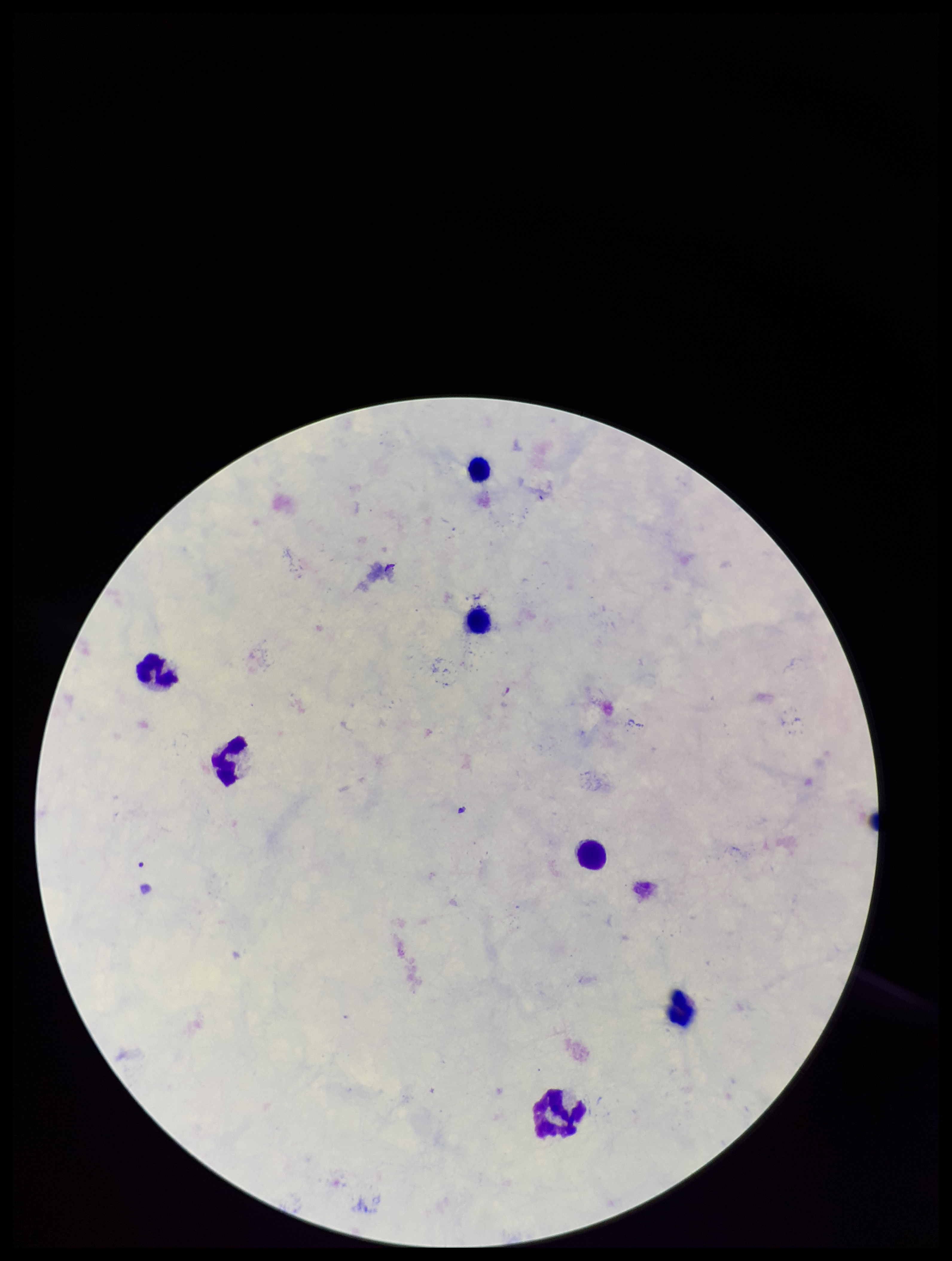

Image is 952×1261 pixels. Leukocyte count: 7. Stained with Giemsa. Patient malaria status: positive. Plasmodium parasites: none detected. Preparation: thick. Parasite count: 0. Single field of view. Species reported for this patient: Plasmodium falciparum. Smartphone photograph taken through the eyepiece of a microscope.